Report the malaria status.
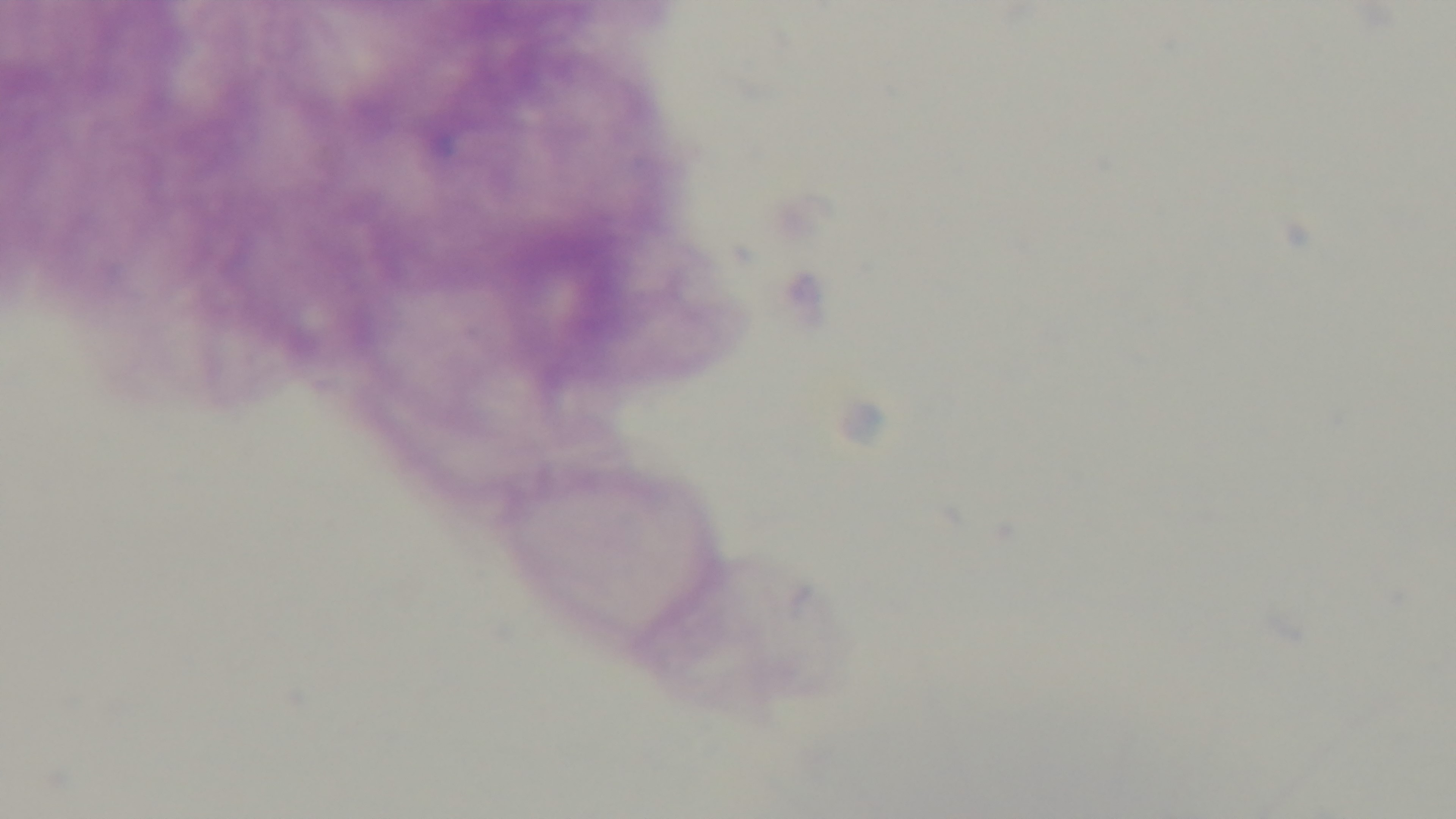

Uninfected.

Summary:
  - Objective: 100x oil immersion
  - Stain: Giemsa
  - Capture: mounted 4K digital camera
  - Modality: light microscopy
  - Preparation: thick
  - Field of view: single